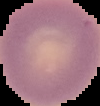

Summary:
  - Preparation: thin blood smear
  - Malaria status: uninfected
  - Image type: segmented cell region on a black background
  - Image size: 100×106 pixels